State the preparation type.
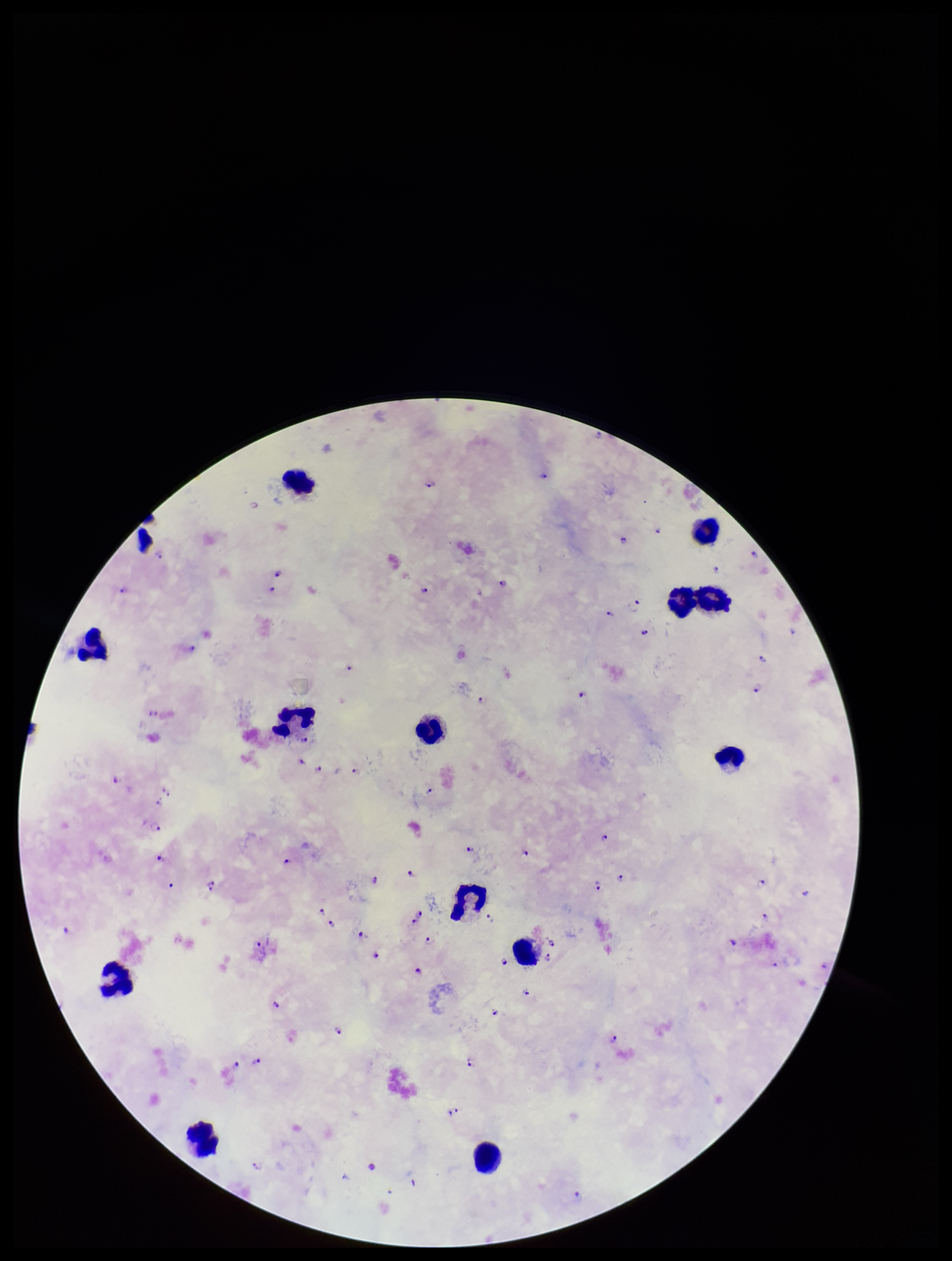
It is a thick blood smear.

capture = smartphone photograph through the microscope eyepiece
leukocyte count = 13
species reported for this patient = Plasmodium falciparum
stain = Giemsa
parasite count = 59
patient malaria status = infected
field of view = single
Plasmodium parasites = seen
image size = 952×1261 pixels